Classify this cell by malaria status.
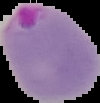

Parasitized.

Summary:
  - Image size: 100×103 pixels
  - Image type: cell region segmented out of the field of view; surrounding area masked to black
  - Preparation: thin blood smear